Give the extent of all Plasmodium parasites.
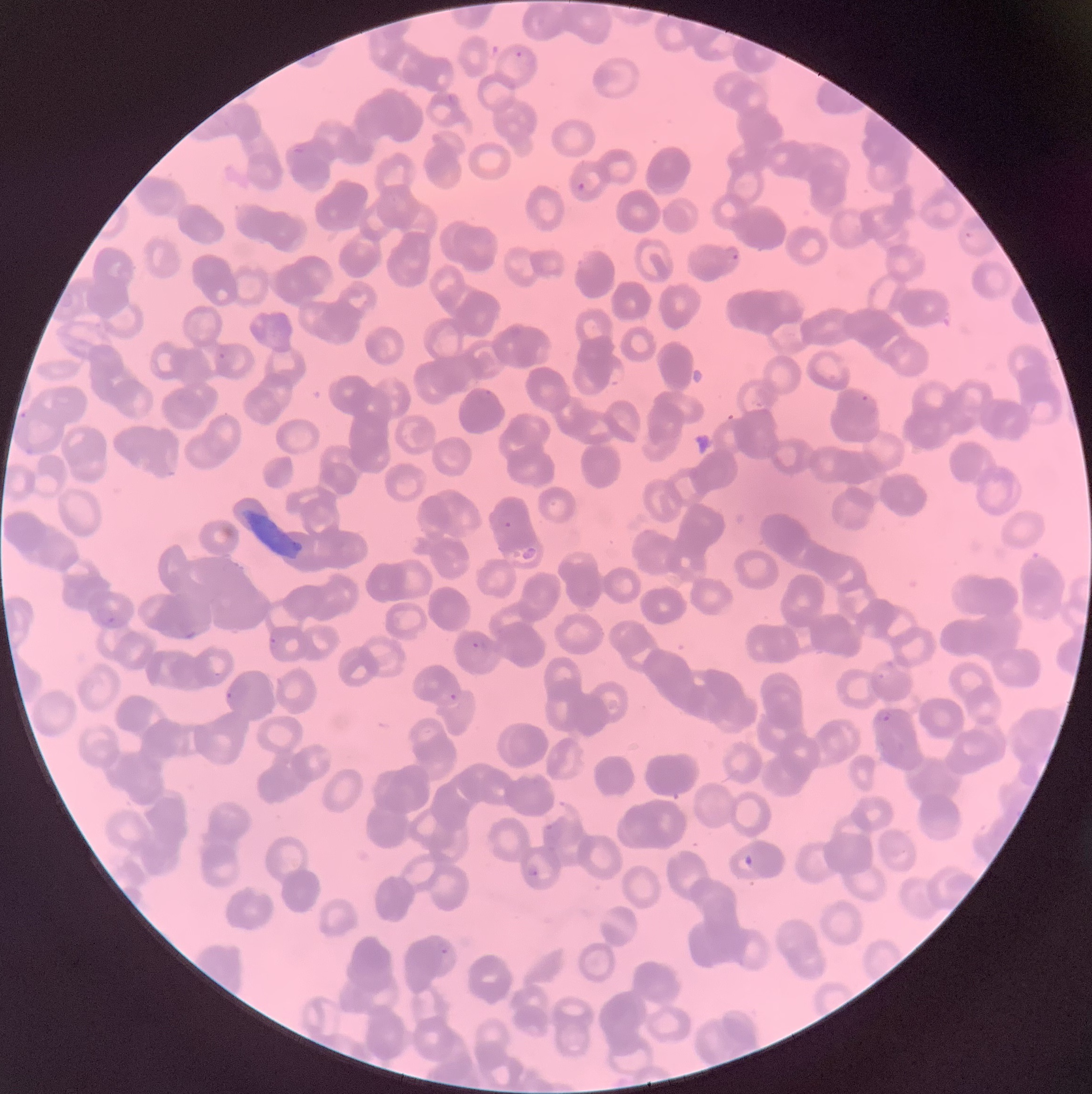

Approximate bounding boxes as [x1, y1, x2, y2] in pixels.
Plasmodium parasites: [515, 51, 523, 58], [447, 92, 459, 105], [291, 142, 308, 156], [578, 182, 585, 190], [726, 246, 739, 261], [219, 350, 226, 358], [608, 364, 626, 387], [859, 393, 878, 412], [20, 409, 28, 420], [23, 446, 35, 457], [499, 513, 514, 530], [98, 607, 115, 625], [268, 636, 279, 649], [469, 639, 487, 651], [877, 673, 886, 681], [226, 687, 239, 702], [449, 692, 459, 700], [878, 709, 891, 720], [548, 801, 570, 826], [524, 863, 539, 877], [436, 937, 451, 956].
Plasmodium parasites too small for a box (approximate centers as [x, y] in pixels): [488, 392], [218, 675].

Summary:
  - Modality: light microscopy
  - Preparation: thin blood smear
  - Red blood cell morphology: rouleaux formation
  - Image size: 1092×1094 pixels